Assess the morphology of the red blood cells.
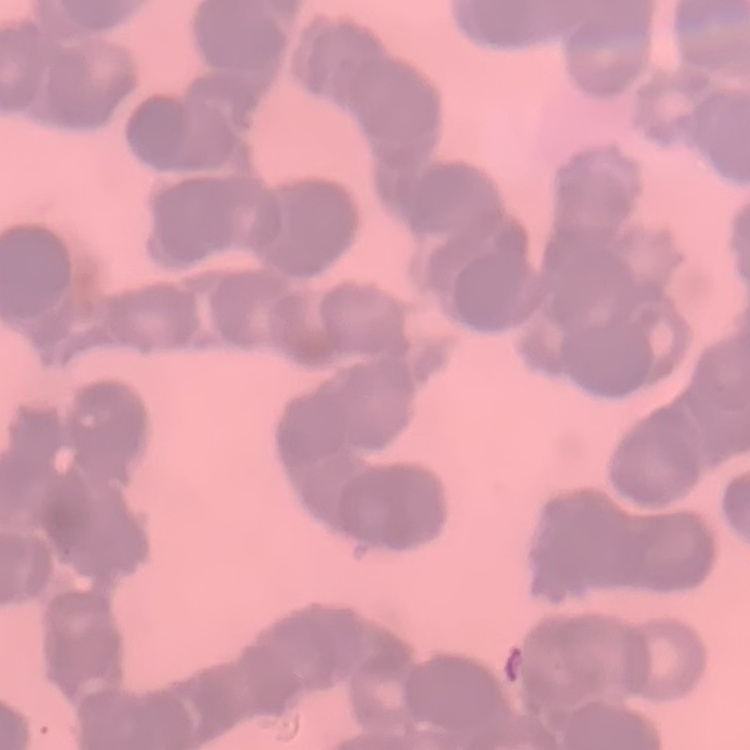
Rouleaux formation.

Summary:
  - Image type: one tile cut from a larger photomicrograph
  - Stain: Field's or Giemsa
  - Preparation: thin blood film